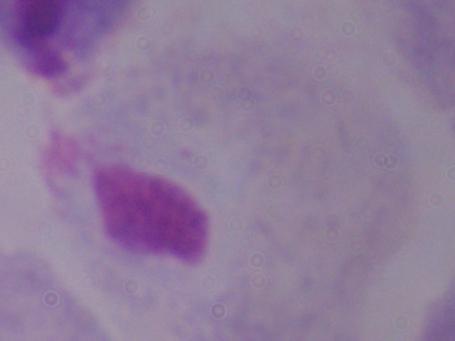
{
  "magnification": "1000x",
  "identification": "trichomonad",
  "modality": "photomicrograph"
}